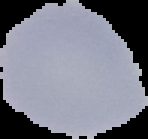
Summary:
  - Image type: segmented cell region on a black background
  - Result: no Plasmodium parasites seen
  - Preparation: thin blood film
  - Image size: 148×139 pixels